Name the cell type shown.
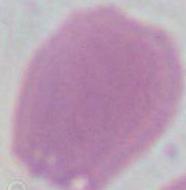
This is an erythrocyte.

Summary:
  - Magnification: 1000x
  - Modality: micrograph